Classify this cell by malaria status.
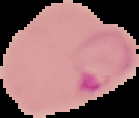
It is parasitized.

Image is 139×118 pixels. Cell region segmented out of the field of view; the surrounding area is masked to black. From a thin blood smear.